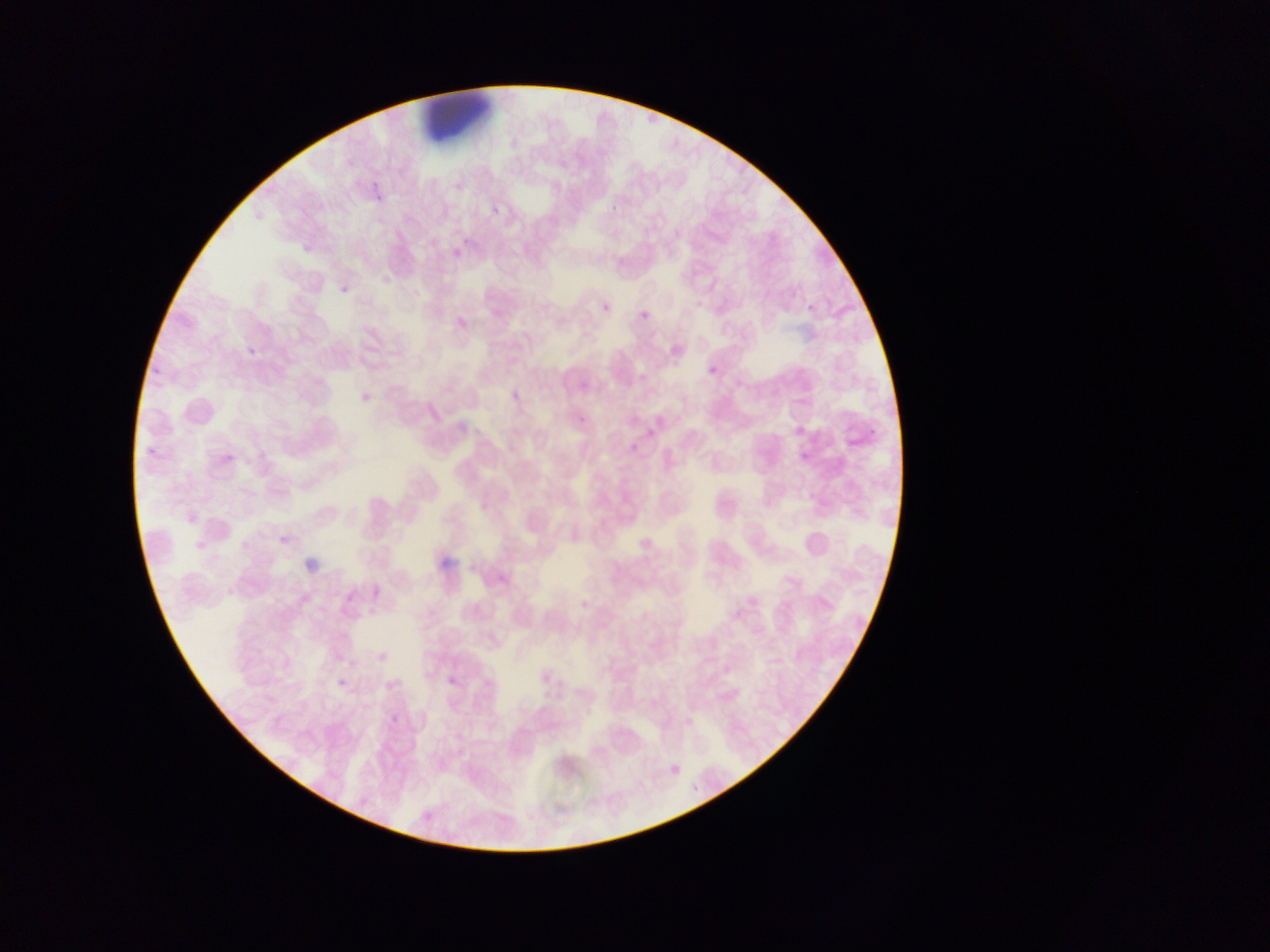
Approximate bounding boxes as {left, top, right, bottom} in pixels.
Summary:
  - Malaria parasite locations: {369, 176, 386, 207}, {492, 206, 501, 215}, {449, 248, 464, 258}, {341, 285, 349, 294}, {452, 302, 472, 323}, {602, 303, 610, 312}, {252, 344, 261, 353}, {708, 366, 717, 375}, {149, 369, 158, 382}, {506, 391, 516, 400}, {363, 392, 372, 402}, {222, 436, 252, 467}, {146, 447, 160, 456}, {272, 526, 298, 542}, {191, 531, 216, 554}, {439, 559, 450, 570}, {468, 562, 477, 572}, {337, 672, 355, 687}, {380, 676, 394, 688}, {440, 679, 456, 690}, {391, 714, 400, 730} | approximate {x, y} pixel centers of objects too small to bound: {459, 184}
  - Country: Ghana
  - Capture: mobile-phone photograph through a microscope
  - Field of view: single
  - Image size: 1270×952 pixels
  - Preparation: thin blood smear